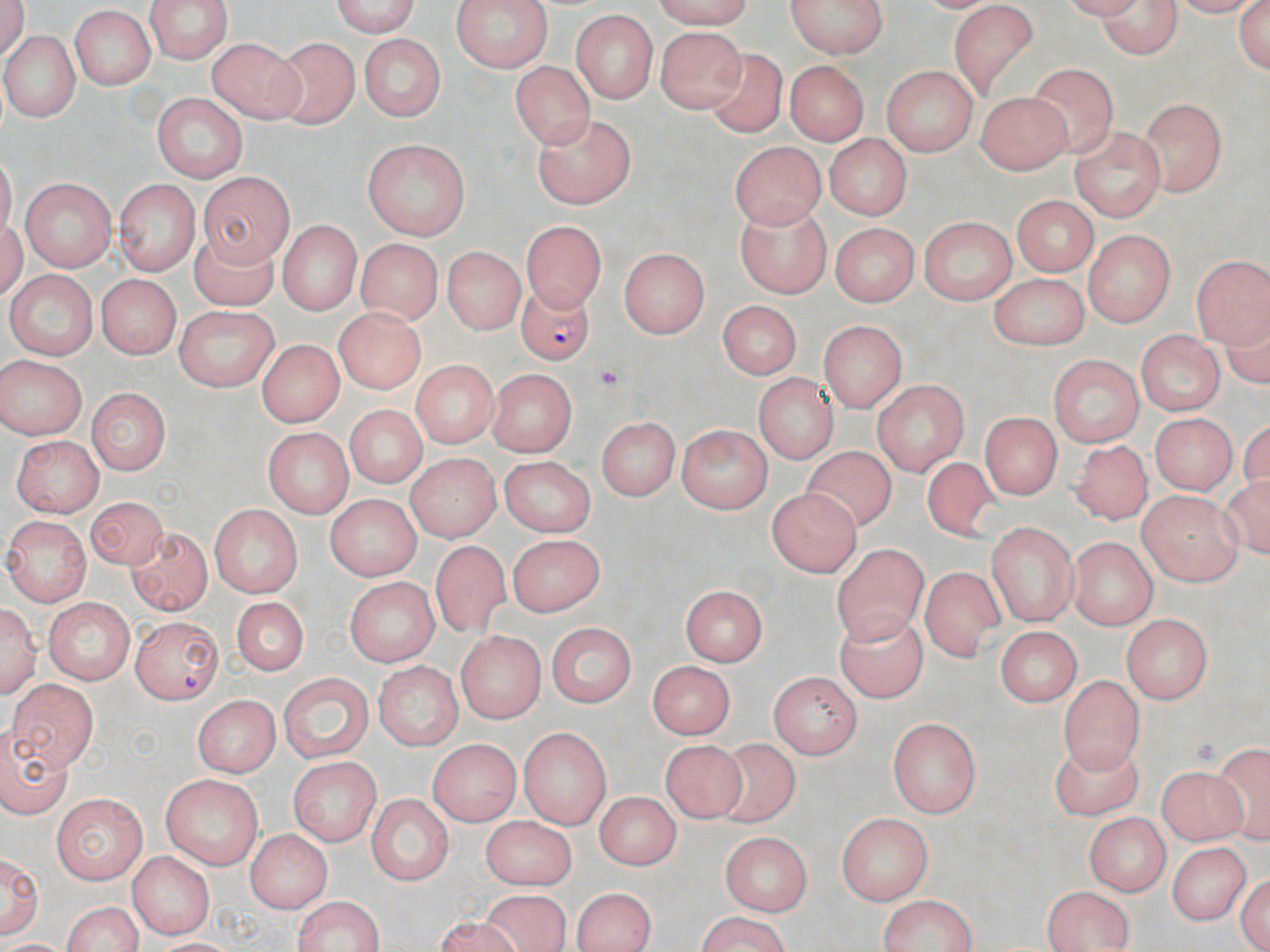

Approximate bounding boxes as (x1,y1)-(x2,y2) corner pairs in pixels. Uninfected red blood cell locations: (143,0)-(236,61), (324,0)-(421,37), (450,0)-(554,73), (649,0)-(755,27), (787,0)-(888,59), (1079,1)-(1184,55), (1234,1)-(1270,77), (949,3)-(1038,93), (71,7)-(157,91), (571,10)-(655,104), (657,27)-(747,112), (6,28)-(77,122), (356,34)-(448,120), (204,36)-(306,120), (274,37)-(358,129), (700,46)-(790,138), (514,60)-(592,149), (785,60)-(867,142), (1029,61)-(1118,160), (880,65)-(978,153), (976,91)-(1068,172), (152,93)-(248,181), (1135,96)-(1226,196), (536,115)-(637,204), (1069,128)-(1167,219), (824,135)-(910,220), (362,138)-(469,240), (730,139)-(828,228), (199,171)-(293,266), (17,176)-(117,269), (115,179)-(199,275), (1010,195)-(1099,274), (736,206)-(830,298), (921,216)-(1017,305), (522,218)-(606,310), (275,221)-(365,314), (833,226)-(915,305), (1084,230)-(1173,325), (188,231)-(279,310), (357,238)-(441,325), (443,247)-(523,337), (619,248)-(709,338), (1192,252)-(1267,347), (8,270)-(97,361), (985,272)-(1090,347), (98,275)-(180,357), (717,303)-(799,382), (175,307)-(279,388), (333,308)-(430,393), (820,321)-(909,408), (1135,329)-(1223,416), (259,338)-(342,426), (0,354)-(87,437), (409,358)-(496,444), (1045,358)-(1143,447), (486,367)-(582,453), (752,375)-(837,463), (871,382)-(970,473), (85,389)-(171,477), (341,405)-(427,489), (978,410)-(1061,497), (1151,413)-(1233,494), (594,417)-(684,499), (676,422)-(771,513), (265,425)-(353,516), (10,433)-(107,515), (1073,439)-(1153,522), (804,447)-(904,535), (402,453)-(497,542), (497,454)-(597,535), (919,456)-(1011,549), (765,489)-(863,576), (1134,491)-(1244,585), (86,493)-(165,571), (325,494)-(422,577), (207,504)-(303,597), (5,516)-(93,604), (987,522)-(1077,625), (122,526)-(213,615), (503,534)-(606,615), (1069,537)-(1157,629), (428,540)-(517,648), (831,540)-(927,642), (921,564)-(1001,664), (344,575)-(437,666), (680,585)-(767,668), (233,594)-(307,675), (42,595)-(132,681), (1,602)-(39,699), (833,605)-(929,705), (1121,613)-(1212,705), (549,620)-(636,705), (992,624)-(1087,705), (456,629)-(544,726), (644,657)-(738,736), (373,660)-(463,749), (277,670)-(375,760), (767,673)-(860,757), (1058,675)-(1143,774), (10,677)-(96,771), (194,698)-(279,776), (890,716)-(982,819), (0,723)-(74,819), (518,724)-(614,825), (429,738)-(521,823), (661,739)-(745,820), (710,740)-(806,829), (1218,741)-(1268,842), (1050,742)-(1144,825), (288,758)-(378,847), (1158,763)-(1246,844), (161,775)-(263,870), (591,791)-(680,869), (367,793)-(452,886), (50,794)-(149,881), (834,811)-(934,902), (483,815)-(576,887), (1088,815)-(1169,892), (246,828)-(332,912), (717,831)-(814,912), (1168,840)-(1251,927), (2,847)-(43,938), (132,852)-(215,938), (1233,868)-(1270,952), (573,885)-(654,952), (1041,886)-(1134,952), (476,890)-(570,952), (876,893)-(977,952), (291,896)-(388,952), (56,897)-(145,952), (689,914)-(795,950). Platelet locations: (592,363)-(622,391). Plasmodium falciparum-infected red blood cell locations: (513,281)-(598,366), (132,616)-(223,701). Slide-level diagnosis: Plasmodium falciparum. Light microscopy. 1000x magnification. Thin blood film. May-Grünwald-Giemsa stain. One field of a larger specimen. Image is 1270×952 pixels.